Assess this cell for malaria.
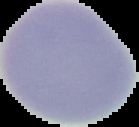

Uninfected.

image type = segmented cell region on a black background
image size = 139×127 pixels
preparation = thin blood smear